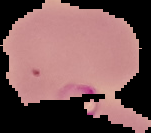

Summary:
  - Image size: 151×133 pixels
  - Image type: segmented cell region with the area outside set to black
  - Result: no Plasmodium parasites detected
  - Preparation: thin blood film